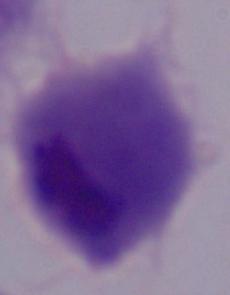 A trichomonad is shown. Micrograph. 1000x magnification.